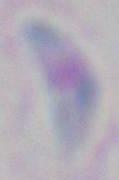
Photomicrograph. Toxoplasma gondii is shown. Captured at 1000x magnification.